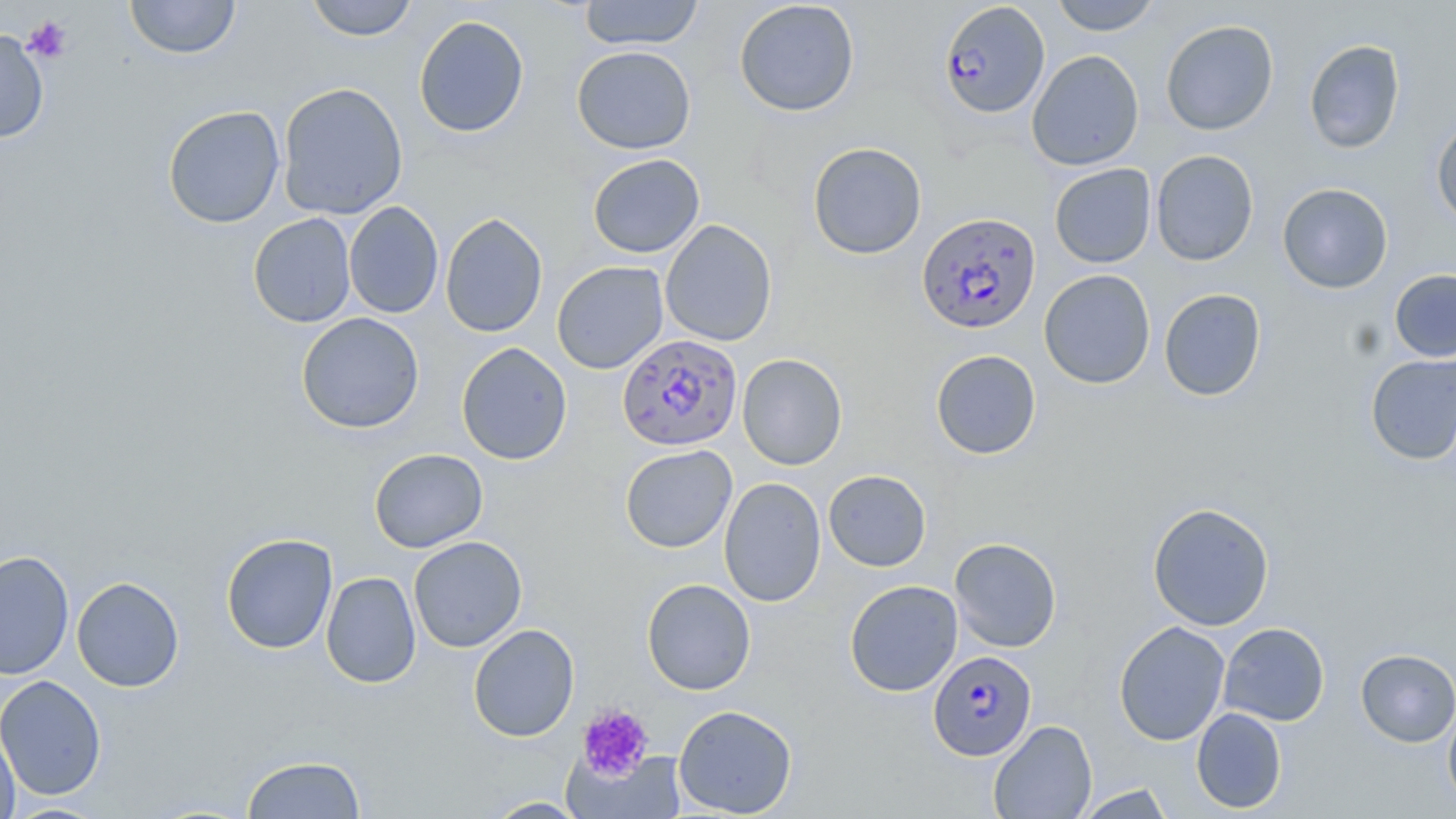 Approximate bounding boxes as (x1,y1)-(x2,y2) corner pairs in pixels. Uninfected red blood cell locations: (124,0)-(241,59), (305,0)-(419,41), (578,0)-(705,51), (1050,0)-(1161,35), (734,1)-(860,116), (413,15)-(529,138), (1160,19)-(1278,136), (0,29)-(49,143), (1303,39)-(1405,154), (571,46)-(696,154), (1026,50)-(1145,170), (277,82)-(408,220), (162,105)-(286,229), (1431,116)-(1456,229), (808,142)-(927,259), (1151,150)-(1259,266), (588,153)-(705,258), (1049,163)-(1157,268), (1277,182)-(1394,294), (344,201)-(444,319), (248,213)-(357,328), (440,213)-(548,338), (660,219)-(777,347), (552,261)-(669,374), (1039,269)-(1156,389), (1389,269)-(1456,362), (1159,288)-(1267,401), (296,312)-(424,434), (456,342)-(573,465), (930,349)-(1041,460), (1365,352)-(1456,466), (737,353)-(848,470), (620,444)-(737,553), (369,448)-(488,553), (823,470)-(931,572), (718,476)-(826,608), (1147,502)-(1274,631), (220,533)-(338,654), (409,536)-(527,652), (949,537)-(1061,652), (0,550)-(75,680), (321,571)-(421,688), (71,576)-(185,692), (641,578)-(756,696), (844,580)-(963,696), (1113,621)-(1231,746), (1218,622)-(1330,726), (468,624)-(580,742), (1355,648)-(1456,747), (0,675)-(107,800), (1442,696)-(1456,813), (673,704)-(798,817), (1191,707)-(1287,814), (0,720)-(20,819), (988,720)-(1097,818), (570,747)-(687,818), (241,754)-(367,818), (1074,783)-(1177,818), (483,797)-(590,818), (5,802)-(111,818). Platelet locations: (23,16)-(73,63), (577,704)-(653,782). Plasmodium falciparum-infected red blood cell locations: (938,2)-(1050,119), (916,211)-(1041,334), (617,333)-(742,452), (928,651)-(1037,762). Slide-level diagnosis: Plasmodium falciparum. 1000x magnification. One field of a larger specimen. Image is 1456×819 pixels. Thin blood film. May-Grünwald-Giemsa-stained preparation. Optical microscopy.